Locate every blood parasite and identify its species.
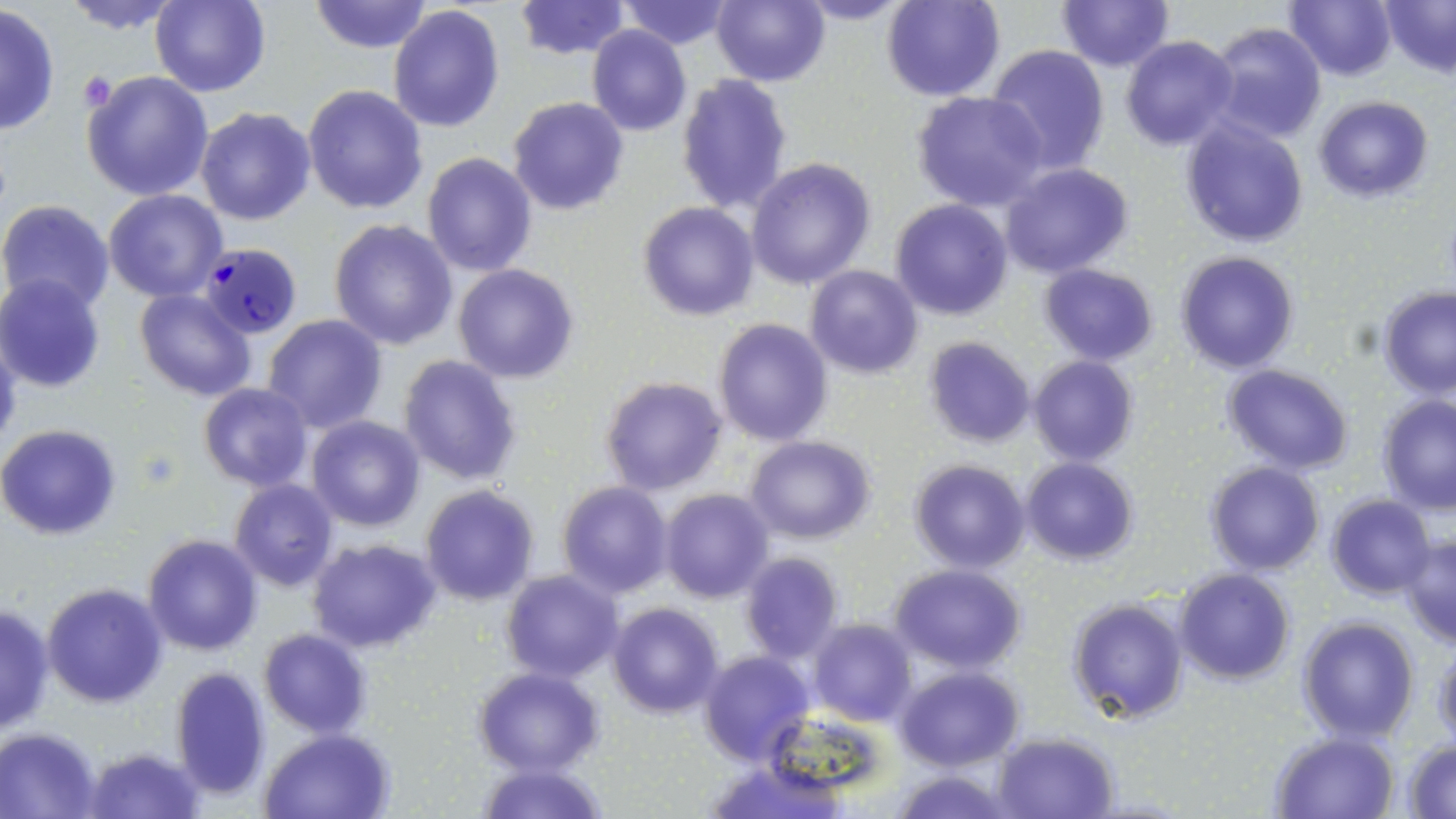
Approximate bounding boxes as (x1,y1)-(x2,y2) corner pairs in pixels.
Plasmodium falciparum-infected red blood cells: (199,242)-(301,340).
No Plasmodium ovale, Plasmodium malariae, Plasmodium vivax, Babesia divergens, or Trypanosoma brucei observed.

Summary:
  - Uninfected red blood cell locations: (60,0)-(186,34), (151,0)-(271,98), (309,0)-(433,54), (617,0)-(733,48), (715,0)-(831,87), (792,0)-(914,25), (881,0)-(1004,102), (1058,0)-(1174,72), (1285,0)-(1396,81), (1381,0)-(1456,77), (515,1)-(631,60), (0,5)-(60,136), (388,6)-(505,132), (1207,22)-(1327,145), (587,27)-(691,136), (1120,36)-(1237,151), (986,44)-(1111,174), (81,71)-(215,201), (678,73)-(793,212), (303,84)-(429,214), (912,92)-(1048,211), (1313,96)-(1433,203), (508,97)-(628,215), (195,107)-(316,226), (1180,118)-(1309,248), (422,153)-(536,276), (746,157)-(875,289), (1001,163)-(1135,278), (103,189)-(229,302), (892,199)-(1013,320), (0,200)-(115,315), (639,202)-(760,321), (329,221)-(458,350), (1175,252)-(1299,374), (1038,264)-(1159,365), (452,265)-(580,384), (806,265)-(923,379), (756,271)-(884,406), (0,276)-(106,392), (1379,287)-(1455,397), (135,289)-(255,401), (262,315)-(387,432), (712,318)-(832,445), (0,326)-(23,454), (923,336)-(1035,449), (398,355)-(522,486), (1028,356)-(1139,467), (1223,364)-(1353,475), (600,376)-(728,495), (199,383)-(313,491), (1376,395)-(1456,514), (308,417)-(424,532), (0,424)-(121,540), (743,436)-(876,543), (1021,457)-(1138,565), (910,459)-(1030,573), (1206,462)-(1325,576), (229,479)-(339,592), (557,482)-(672,598), (419,485)-(539,606), (660,488)-(774,603), (168,493)-(289,628), (1326,495)-(1435,600), (1399,533)-(1456,648), (144,534)-(263,656), (307,538)-(443,654), (739,552)-(844,661), (890,565)-(1025,672), (1174,568)-(1294,684), (500,571)-(624,681), (43,582)-(167,706), (1067,597)-(1189,723), (609,602)-(724,717), (0,604)-(55,737), (1297,616)-(1419,741), (807,619)-(916,725), (259,628)-(371,739), (1431,645)-(1456,748), (698,650)-(814,766), (169,665)-(273,799), (894,666)-(1023,770), (474,667)-(604,776), (0,728)-(102,817), (994,730)-(1119,818), (263,731)-(392,818), (1270,731)-(1398,817), (1402,740)-(1456,817), (82,746)-(205,819), (476,761)-(607,818), (889,770)-(1019,818)
  - Platelet locations: (79,73)-(116,114)
  - Slide-level diagnosis: Plasmodium falciparum
  - Field of view: single
  - Stain: May-Grünwald-Giemsa
  - Modality: light microscopy
  - Preparation: thin blood film
  - Image size: 1456×819 pixels
  - Magnification: 1000x